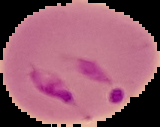
Summary:
  - Result: malaria parasites identified
  - Image size: 160×127 pixels
  - Preparation: thin blood film
  - Image type: segmented cell region with the area outside set to black